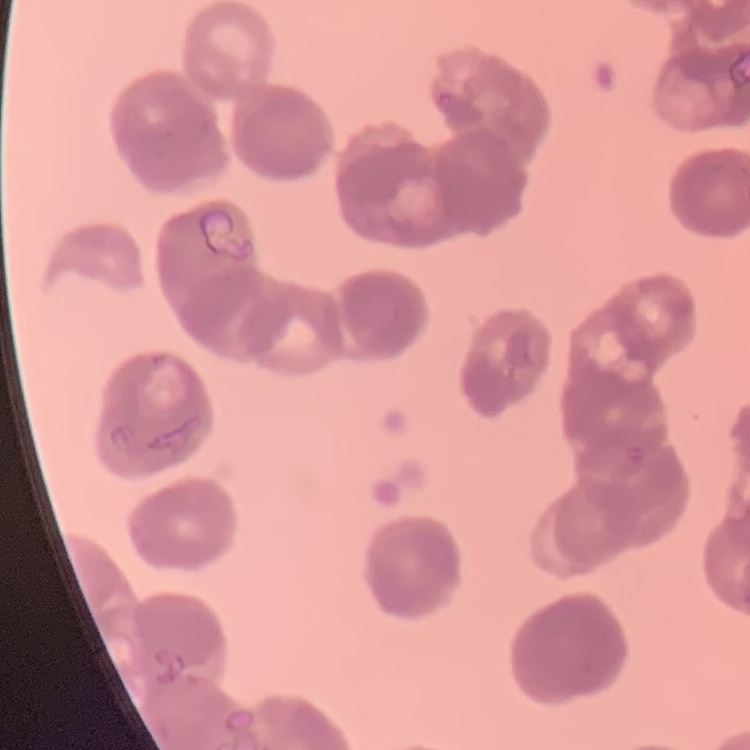

red blood cell morphology = rouleaux formation
preparation = thin blood smear
image type = one tile cut from a larger photomicrograph
stain = Field's or Giemsa